State the preparation type.
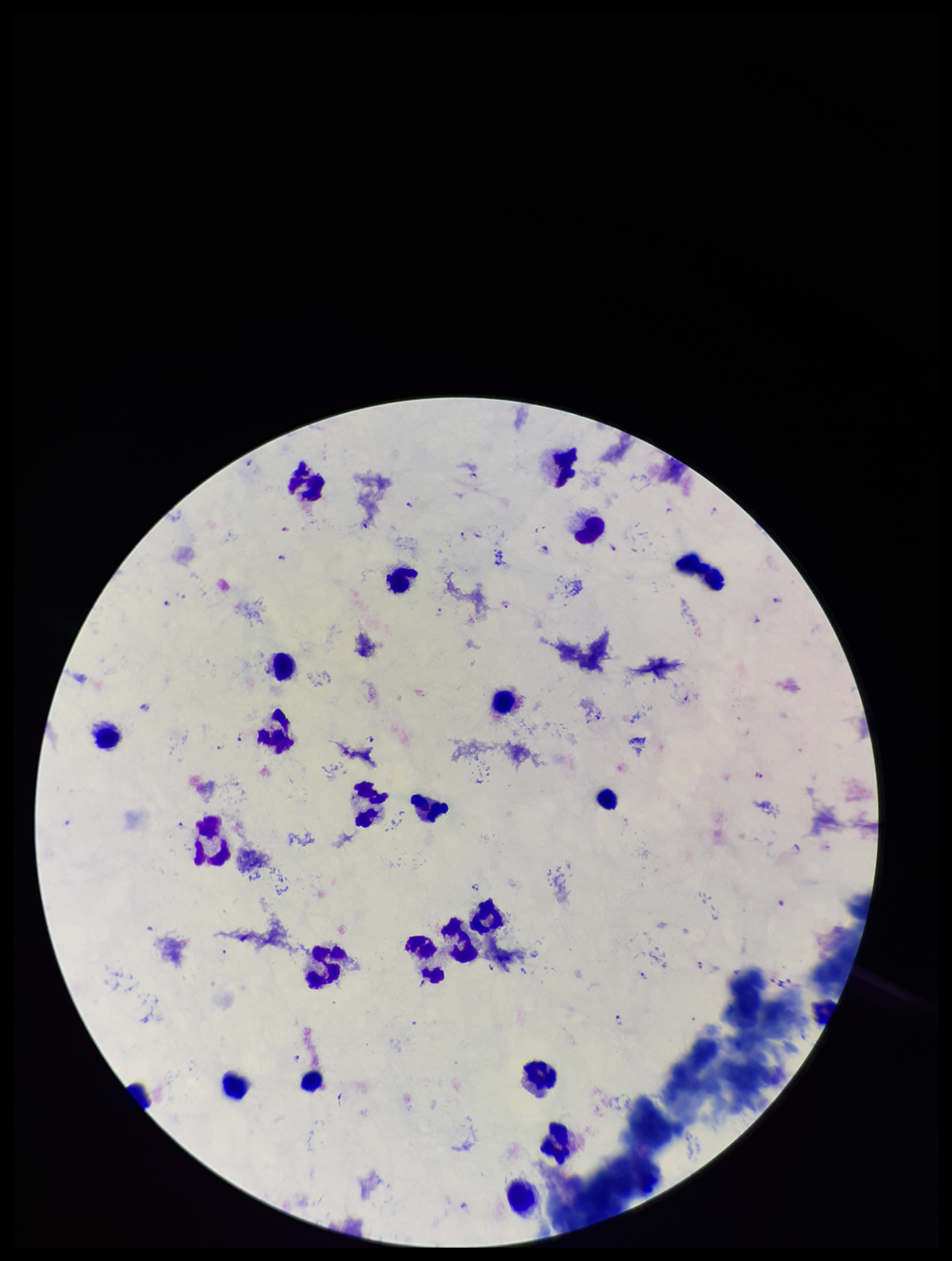
Thick.

Summary:
  - Stain: Giemsa
  - Plasmodium parasites: seen
  - Image size: 952×1261 pixels
  - Field of view: one from this slide
  - Species reported for this patient: Plasmodium falciparum
  - Parasite count: 31
  - Leukocyte count: 23
  - Capture: smartphone photograph through the microscope eyepiece
  - Patient malaria status: positive